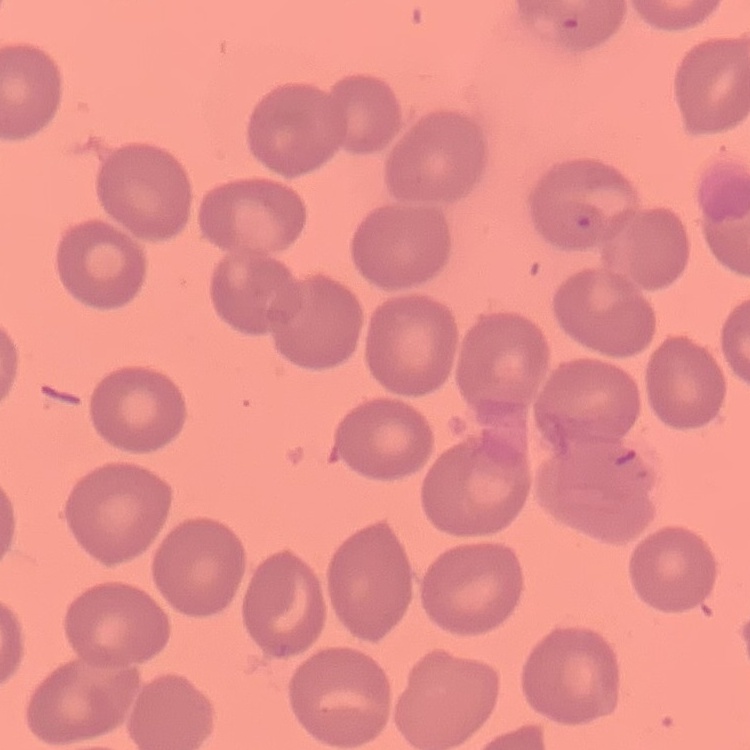

The erythrocytes exhibit no rouleaux formation. Field's or Giemsa stain. Thin blood smear. Square crop of a larger photomicrograph.